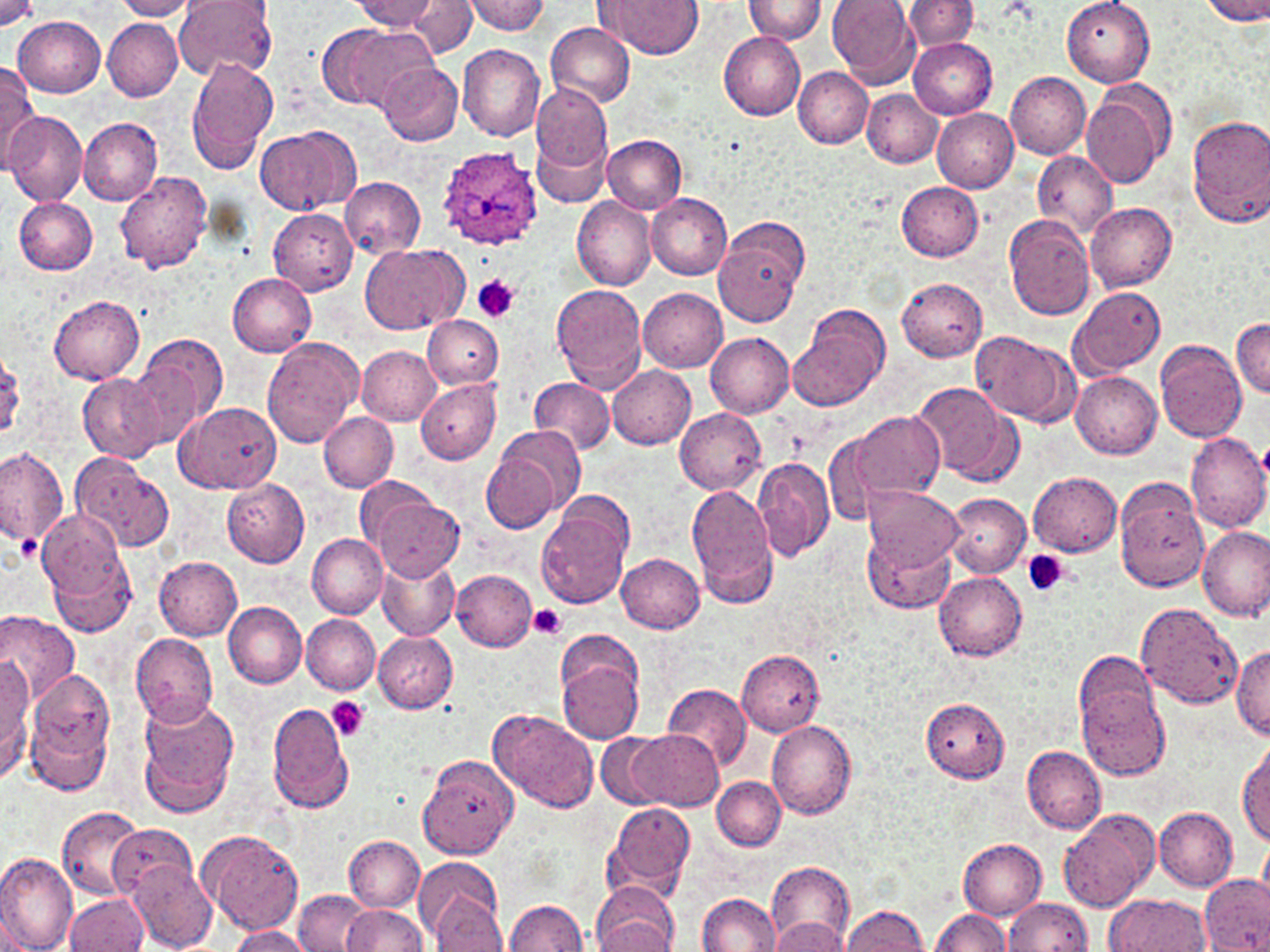
Plasmodium ovale-infected red blood cell locations = approximate bounding boxes as named x1/y1/x2/y2 corners in pixels: (x1=433, y1=148, x2=541, y2=251)
slide-level diagnosis = Plasmodium ovale
platelet locations = approximate bounding boxes as named x1/y1/x2/y2 corners in pixels: (x1=473, y1=274, x2=520, y2=322), (x1=10, y1=534, x2=37, y2=564), (x1=1023, y1=551, x2=1069, y2=598), (x1=528, y1=604, x2=565, y2=641), (x1=326, y1=697, x2=370, y2=741)
image size = 1270×952 pixels
field of view = one of a larger specimen
magnification = 1000x
modality = light microscopy
uninfected red blood cell locations = approximate bounding boxes as named x1/y1/x2/y2 corners in pixels: (x1=113, y1=0, x2=199, y2=19), (x1=173, y1=0, x2=278, y2=81), (x1=354, y1=0, x2=440, y2=33), (x1=408, y1=0, x2=478, y2=57), (x1=465, y1=0, x2=549, y2=36), (x1=600, y1=0, x2=702, y2=58), (x1=827, y1=0, x2=919, y2=86), (x1=902, y1=0, x2=979, y2=53), (x1=1061, y1=0, x2=1157, y2=86), (x1=1199, y1=0, x2=1270, y2=24), (x1=0, y1=1, x2=37, y2=29), (x1=743, y1=1, x2=829, y2=43), (x1=13, y1=16, x2=106, y2=96), (x1=102, y1=18, x2=181, y2=101), (x1=546, y1=22, x2=635, y2=108), (x1=316, y1=24, x2=427, y2=111), (x1=719, y1=32, x2=806, y2=119), (x1=909, y1=39, x2=997, y2=118), (x1=457, y1=42, x2=545, y2=141), (x1=186, y1=57, x2=279, y2=174), (x1=377, y1=62, x2=462, y2=145), (x1=0, y1=64, x2=38, y2=167), (x1=792, y1=66, x2=873, y2=148), (x1=1007, y1=72, x2=1091, y2=160), (x1=1083, y1=79, x2=1177, y2=192), (x1=532, y1=84, x2=612, y2=198), (x1=863, y1=90, x2=942, y2=166), (x1=932, y1=108, x2=1019, y2=193), (x1=3, y1=111, x2=86, y2=204), (x1=1187, y1=115, x2=1270, y2=227), (x1=78, y1=118, x2=164, y2=205), (x1=256, y1=126, x2=360, y2=216), (x1=603, y1=133, x2=686, y2=214), (x1=1032, y1=151, x2=1117, y2=240), (x1=116, y1=171, x2=213, y2=275), (x1=341, y1=176, x2=426, y2=258), (x1=897, y1=182, x2=984, y2=262), (x1=645, y1=192, x2=732, y2=279), (x1=13, y1=195, x2=98, y2=274), (x1=572, y1=198, x2=656, y2=290), (x1=1085, y1=202, x2=1178, y2=292), (x1=268, y1=208, x2=358, y2=294), (x1=1004, y1=214, x2=1096, y2=320), (x1=714, y1=228, x2=805, y2=328), (x1=361, y1=244, x2=461, y2=335), (x1=228, y1=273, x2=317, y2=356), (x1=897, y1=278, x2=987, y2=361), (x1=551, y1=284, x2=647, y2=392), (x1=1071, y1=286, x2=1166, y2=376), (x1=637, y1=287, x2=728, y2=372), (x1=49, y1=295, x2=145, y2=384), (x1=789, y1=305, x2=889, y2=410), (x1=423, y1=314, x2=503, y2=389), (x1=1232, y1=317, x2=1270, y2=398), (x1=1112, y1=327, x2=1224, y2=431), (x1=968, y1=331, x2=1078, y2=428), (x1=706, y1=333, x2=794, y2=417), (x1=136, y1=334, x2=229, y2=439), (x1=262, y1=338, x2=363, y2=448), (x1=1155, y1=339, x2=1246, y2=443), (x1=357, y1=346, x2=440, y2=426), (x1=0, y1=352, x2=25, y2=441), (x1=608, y1=366, x2=696, y2=449), (x1=1071, y1=372, x2=1162, y2=460), (x1=78, y1=373, x2=168, y2=464), (x1=415, y1=378, x2=501, y2=464), (x1=530, y1=378, x2=614, y2=455), (x1=911, y1=380, x2=1019, y2=485), (x1=426, y1=386, x2=546, y2=485), (x1=175, y1=400, x2=283, y2=495), (x1=676, y1=408, x2=767, y2=495), (x1=850, y1=409, x2=943, y2=503), (x1=318, y1=412, x2=399, y2=493), (x1=480, y1=430, x2=580, y2=536), (x1=821, y1=431, x2=886, y2=530), (x1=1186, y1=432, x2=1270, y2=533), (x1=0, y1=445, x2=69, y2=550), (x1=69, y1=452, x2=174, y2=553), (x1=752, y1=456, x2=833, y2=562), (x1=702, y1=466, x2=816, y2=581), (x1=1029, y1=472, x2=1123, y2=557), (x1=221, y1=477, x2=310, y2=565), (x1=1114, y1=478, x2=1209, y2=593), (x1=358, y1=479, x2=443, y2=558), (x1=688, y1=483, x2=779, y2=607), (x1=946, y1=483, x2=1118, y2=564), (x1=863, y1=484, x2=964, y2=573), (x1=945, y1=493, x2=1031, y2=576), (x1=370, y1=496, x2=465, y2=581), (x1=536, y1=504, x2=630, y2=609), (x1=37, y1=510, x2=133, y2=610), (x1=1198, y1=527, x2=1268, y2=623), (x1=307, y1=531, x2=385, y2=618), (x1=864, y1=532, x2=956, y2=614), (x1=47, y1=550, x2=138, y2=638), (x1=617, y1=553, x2=704, y2=633), (x1=376, y1=555, x2=459, y2=640), (x1=155, y1=556, x2=243, y2=640), (x1=451, y1=569, x2=536, y2=651), (x1=934, y1=571, x2=1027, y2=661), (x1=223, y1=601, x2=307, y2=689), (x1=1136, y1=602, x2=1242, y2=711), (x1=0, y1=609, x2=80, y2=707), (x1=302, y1=615, x2=380, y2=694), (x1=131, y1=632, x2=218, y2=725), (x1=373, y1=632, x2=458, y2=712), (x1=1232, y1=645, x2=1270, y2=739), (x1=556, y1=646, x2=645, y2=745), (x1=737, y1=650, x2=825, y2=736), (x1=1073, y1=651, x2=1161, y2=739), (x1=0, y1=658, x2=33, y2=779), (x1=24, y1=676, x2=115, y2=795), (x1=1076, y1=676, x2=1169, y2=781), (x1=662, y1=684, x2=751, y2=771), (x1=136, y1=695, x2=239, y2=815), (x1=919, y1=697, x2=1011, y2=783), (x1=267, y1=701, x2=355, y2=815), (x1=490, y1=711, x2=600, y2=815), (x1=766, y1=720, x2=859, y2=819), (x1=629, y1=730, x2=722, y2=812), (x1=597, y1=731, x2=667, y2=809), (x1=1238, y1=744, x2=1270, y2=848), (x1=1022, y1=745, x2=1107, y2=834), (x1=419, y1=756, x2=518, y2=859), (x1=713, y1=777, x2=786, y2=850), (x1=605, y1=802, x2=695, y2=901), (x1=57, y1=805, x2=145, y2=899), (x1=1154, y1=807, x2=1238, y2=891), (x1=1057, y1=808, x2=1160, y2=913), (x1=109, y1=823, x2=200, y2=903), (x1=197, y1=829, x2=305, y2=935), (x1=345, y1=836, x2=425, y2=911), (x1=1259, y1=836, x2=1270, y2=906), (x1=960, y1=839, x2=1047, y2=920), (x1=0, y1=849, x2=77, y2=952), (x1=415, y1=857, x2=503, y2=940), (x1=128, y1=861, x2=216, y2=951), (x1=768, y1=863, x2=855, y2=947), (x1=1199, y1=873, x2=1270, y2=952), (x1=591, y1=881, x2=679, y2=952), (x1=294, y1=890, x2=370, y2=952), (x1=696, y1=892, x2=779, y2=951), (x1=64, y1=893, x2=147, y2=951), (x1=1106, y1=893, x2=1211, y2=952), (x1=432, y1=897, x2=507, y2=950), (x1=505, y1=898, x2=587, y2=951), (x1=1004, y1=898, x2=1093, y2=952), (x1=343, y1=903, x2=428, y2=951), (x1=841, y1=904, x2=927, y2=952), (x1=931, y1=909, x2=1012, y2=952), (x1=772, y1=916, x2=850, y2=952), (x1=226, y1=926, x2=313, y2=952)
stain = May-Grünwald-Giemsa
preparation = thin blood film